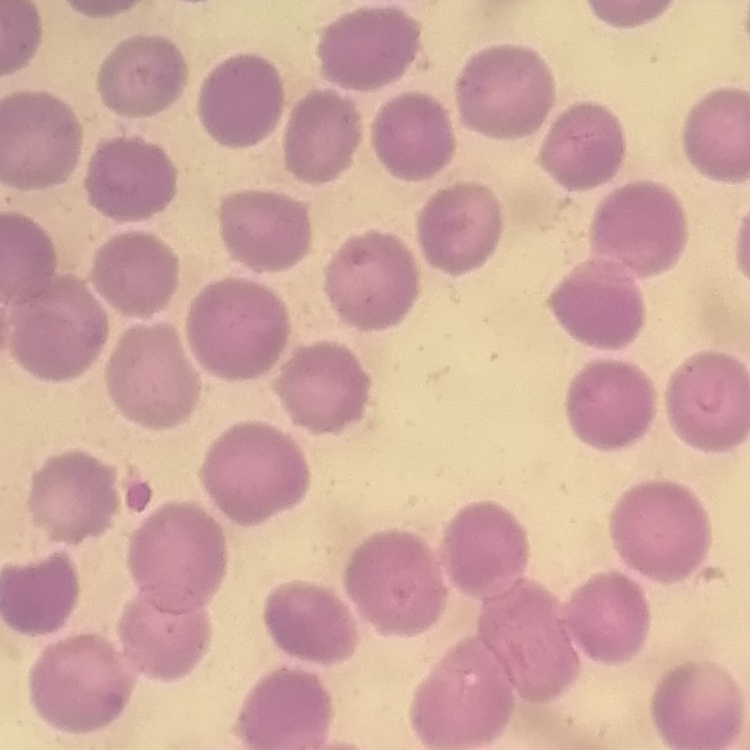

Summary:
  - Erythrocyte morphology: no rouleaux formation
  - Image type: one tile cut from a larger photomicrograph
  - Stain: Field's or Giemsa
  - Preparation: thin blood film